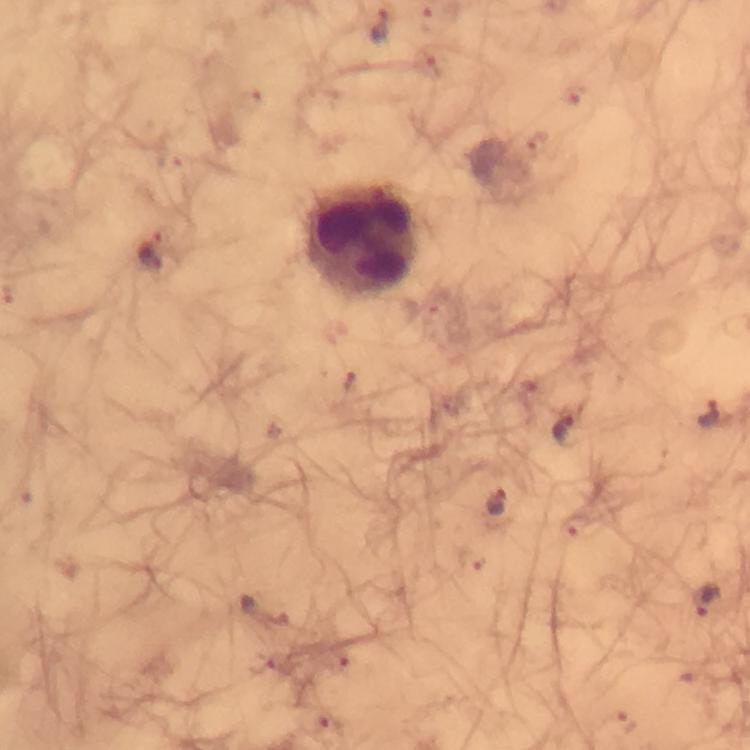

Approximate centers as (x, y) in pixels. Malaria parasite locations: (379, 26), (153, 251), (350, 384), (708, 413), (565, 428), (495, 502), (705, 599). Leukocyte locations: (362, 241). Giemsa-stained preparation. Thick blood film. Image is 750×750 pixels. From a diagnostic examination for malaria. At 100x magnification. Immersion oil was used. Photographed with a smartphone mounted on the microscope. Cropped region of a single field of view.